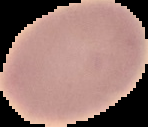

Summary:
  - Image size: 148×127 pixels
  - Preparation: thin blood smear
  - Image type: cell region segmented out of the field of view; surrounding area masked to black
  - Result: negative for Plasmodium parasites